Classify this cell by malaria status.
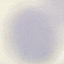

Uninfected.

Summary:
  - Image type: cell patch, automatically extracted from a larger field of view and resized to 64 × 64 pixels
  - Preparation: thin smear
  - Stain: Giemsa
  - Capture: smartphone through the microscope eyepiece